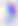
Micrograph. Toxoplasma gondii is seen. 400x magnification.